Comment on the morphology of the erythrocytes.
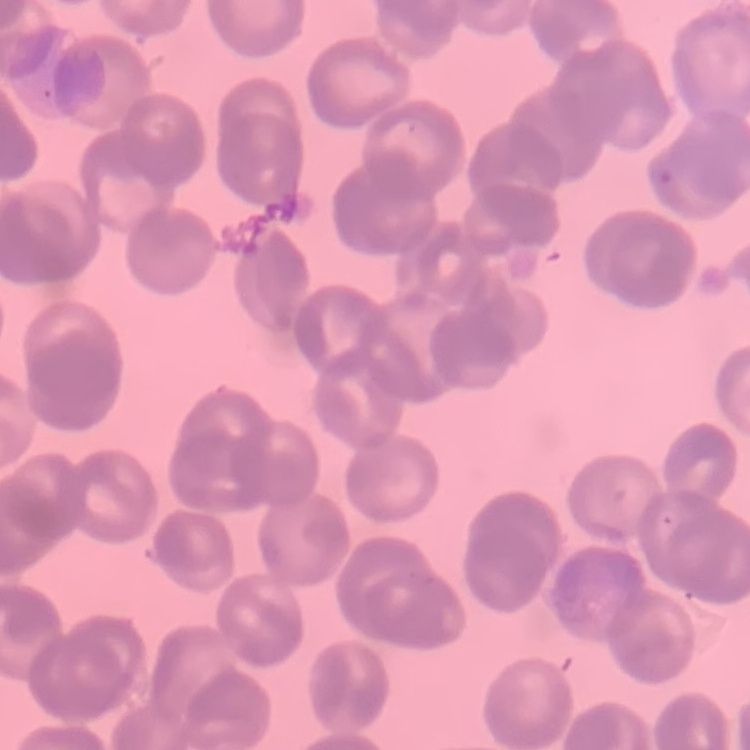
They show rouleaux formation.

Thin blood smear. One tile cut from a larger photomicrograph. Stained with either Field's or Giemsa.